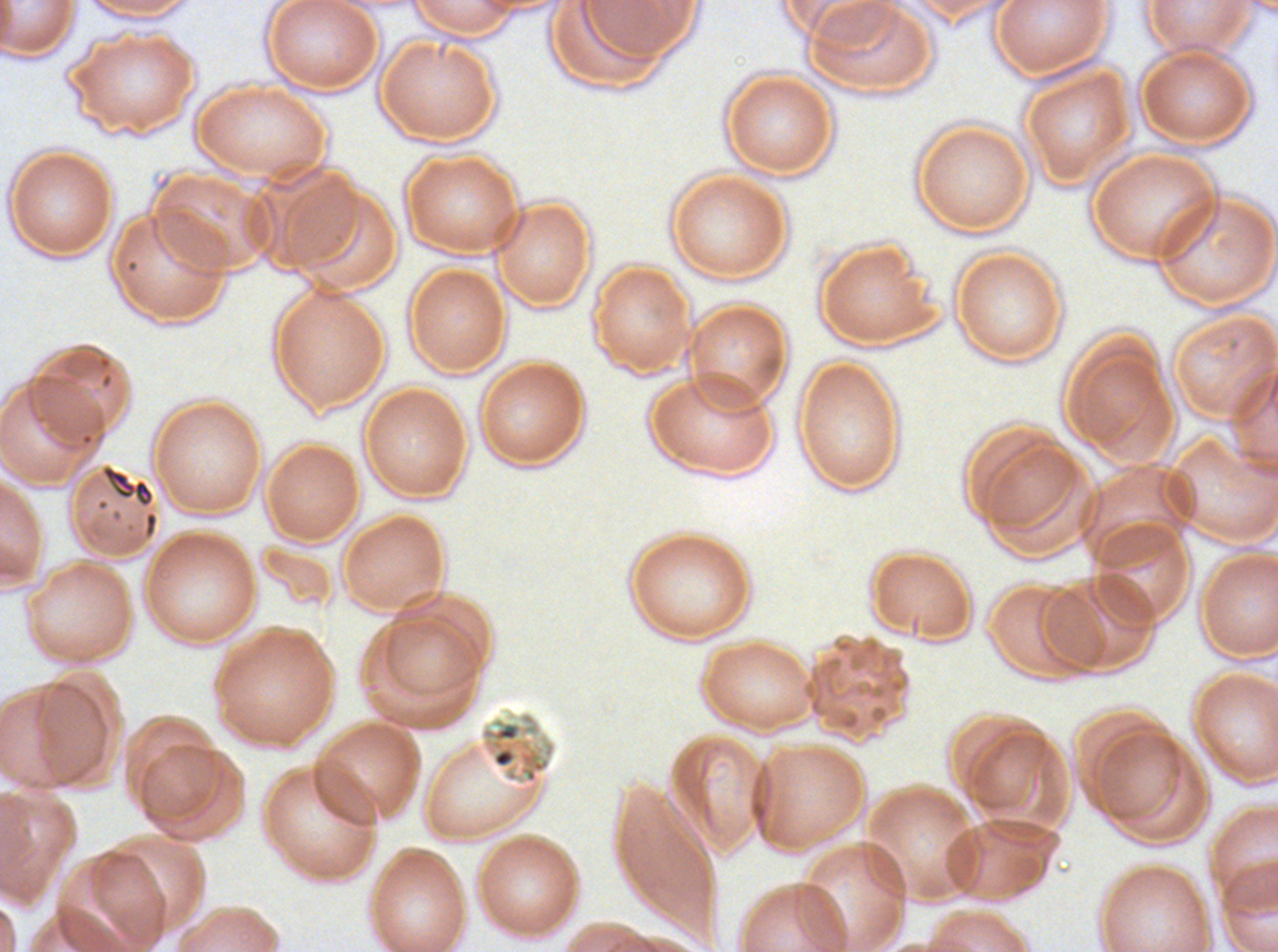

Approximate bounding boxes as {x1, y1, x2, y2} in pixels.
Summary:
  - Debris locations: {98, 462, 156, 510}, {479, 711, 557, 803}
  - Specimen: P. falciparum from a patient in The Gambia, cultured ex vivo for 24 to 48 hours
  - Field of view: one sub-image of a larger composite
  - Image size: 1278×952 pixels
  - Stain: Giemsa
  - Preparation: thin blood smear